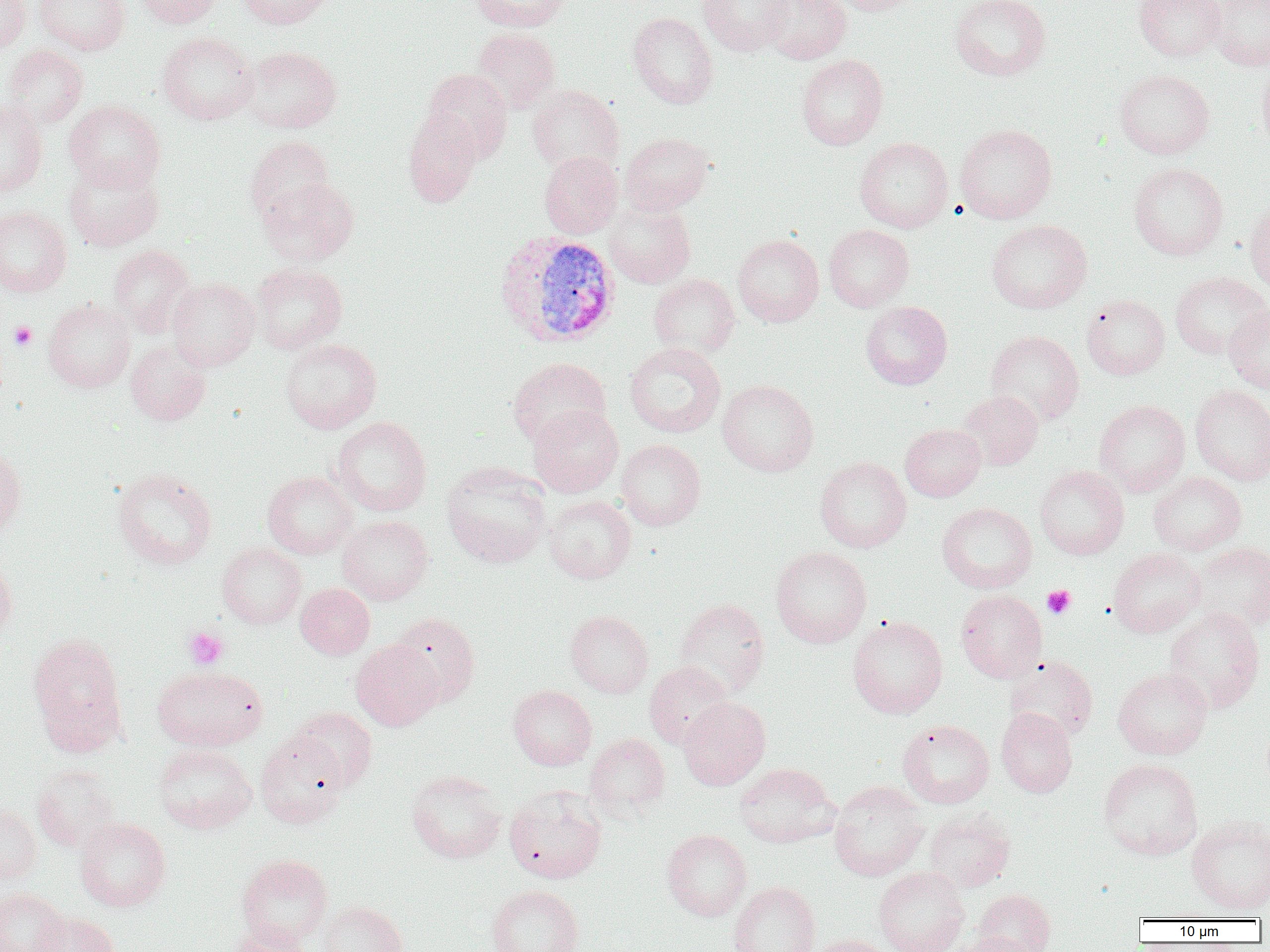

slide-level diagnosis = Plasmodium vivax
modality = optical microscopy
uninfected red blood cell locations = approximate bounding boxes as (x1,y1)-(x2,y2) corner pairs in pixels: (0,0)-(32,53), (34,0)-(131,55), (132,0)-(223,28), (239,0)-(335,28), (470,0)-(572,32), (699,0)-(791,57), (761,0)-(850,64), (831,0)-(923,15), (950,0)-(1052,81), (1133,0)-(1225,61), (1205,1)-(1270,70), (628,12)-(718,109), (471,27)-(560,114), (157,31)-(260,125), (2,45)-(88,128), (240,45)-(341,133), (796,54)-(888,150), (1257,60)-(1270,156), (421,68)-(513,163), (1114,68)-(1215,159), (527,85)-(624,176), (0,99)-(48,198), (63,100)-(166,191), (403,111)-(482,208), (955,123)-(1057,224), (620,132)-(714,215), (245,136)-(335,225), (854,137)-(953,233), (539,151)-(623,238), (63,158)-(164,252), (1128,162)-(1228,260), (259,177)-(359,266), (1245,200)-(1270,295), (603,201)-(695,288), (0,206)-(72,296), (986,219)-(1092,313), (823,224)-(914,312), (733,234)-(824,327), (107,244)-(198,337), (250,262)-(347,354), (1170,271)-(1269,360), (648,274)-(740,357), (167,278)-(260,370), (1081,294)-(1170,380), (43,299)-(135,392), (860,301)-(952,390), (1224,304)-(1270,394), (986,330)-(1084,425), (280,338)-(381,433), (126,340)-(211,425), (625,343)-(726,438), (507,357)-(611,448), (717,380)-(818,477), (1190,385)-(1270,485), (957,390)-(1043,470), (1094,399)-(1190,496), (528,405)-(623,497), (331,416)-(431,516), (900,423)-(986,501), (616,439)-(706,530), (0,446)-(26,538), (815,456)-(911,553), (441,462)-(551,568), (1035,466)-(1129,560), (112,468)-(218,568), (262,470)-(358,559), (1148,472)-(1246,556), (544,495)-(636,583), (937,502)-(1037,593), (337,514)-(433,605), (1190,542)-(1270,631), (217,543)-(306,629), (770,546)-(872,648), (1109,548)-(1205,637), (0,557)-(17,644), (296,583)-(374,659), (956,589)-(1047,683), (674,597)-(770,697), (1164,607)-(1265,712), (565,609)-(654,698), (390,612)-(480,707), (847,615)-(948,718), (27,633)-(127,752), (350,639)-(444,730), (1004,655)-(1098,741), (644,661)-(733,750), (152,665)-(267,751), (1113,667)-(1213,759), (508,685)-(596,770), (678,697)-(770,790), (291,706)-(378,791), (996,707)-(1077,797), (897,719)-(994,808), (255,730)-(350,829), (585,733)-(670,819), (153,743)-(256,834), (1098,758)-(1203,860), (734,762)-(840,847), (32,764)-(121,852), (406,769)-(507,863), (828,781)-(930,881), (504,786)-(607,884), (0,803)-(42,884), (923,809)-(1016,892), (1187,816)-(1270,915), (74,817)-(171,911), (662,829)-(752,921), (236,854)-(332,946), (873,866)-(969,952), (728,880)-(820,952), (486,884)-(584,952), (0,887)-(70,952), (973,888)-(1056,952), (318,900)-(407,952), (33,912)-(120,952), (228,922)-(315,952), (950,931)-(1039,952), (808,934)-(893,952)
platelet locations = approximate bounding boxes as (x1,y1)-(x2,y2) corner pairs in pixels: (9,321)-(37,350), (1042,585)-(1076,619), (183,626)-(229,670)
magnification = 1000x
field of view = one of a larger specimen
image size = 1270×952 pixels
Plasmodium vivax-infected red blood cell locations = approximate bounding boxes as (x1,y1)-(x2,y2) corner pairs in pixels: (493,230)-(621,348)
preparation = thin blood film